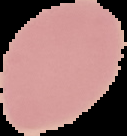
image type = cell region segmented out of the field of view; surrounding area masked to black
result = no Plasmodium parasites detected
image size = 127×136 pixels
preparation = thin blood smear